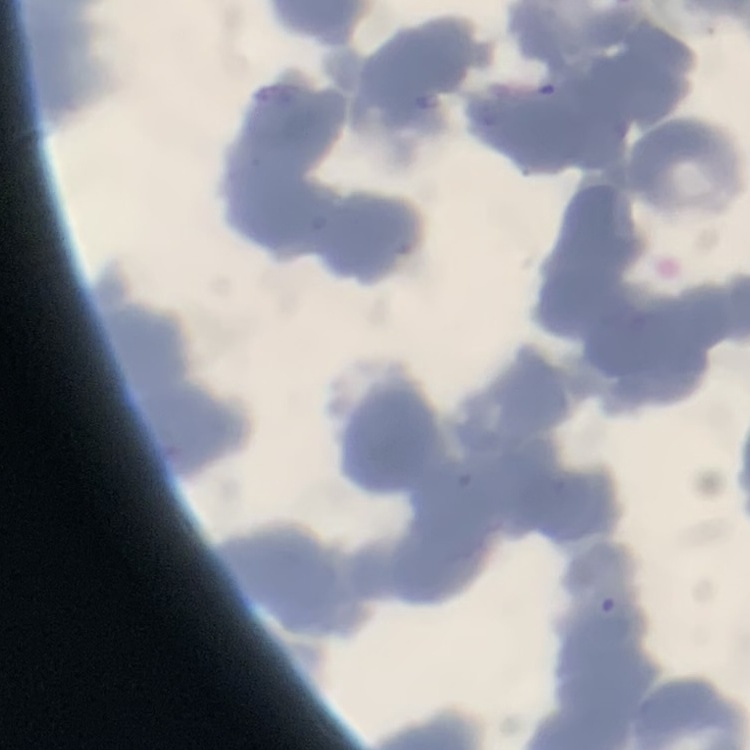

erythrocyte_morphology: rouleaux formation
stain: Field's or Giemsa
image_type: square crop of a larger photomicrograph
preparation: thin peripheral smear